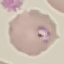 Result: malaria parasites identified. Giemsa stain. Thin blood smear. Photographed with a smartphone camera at the microscope eyepiece. Cell patch, automatically extracted from a larger field of view and resized to 64 × 64 pixels.